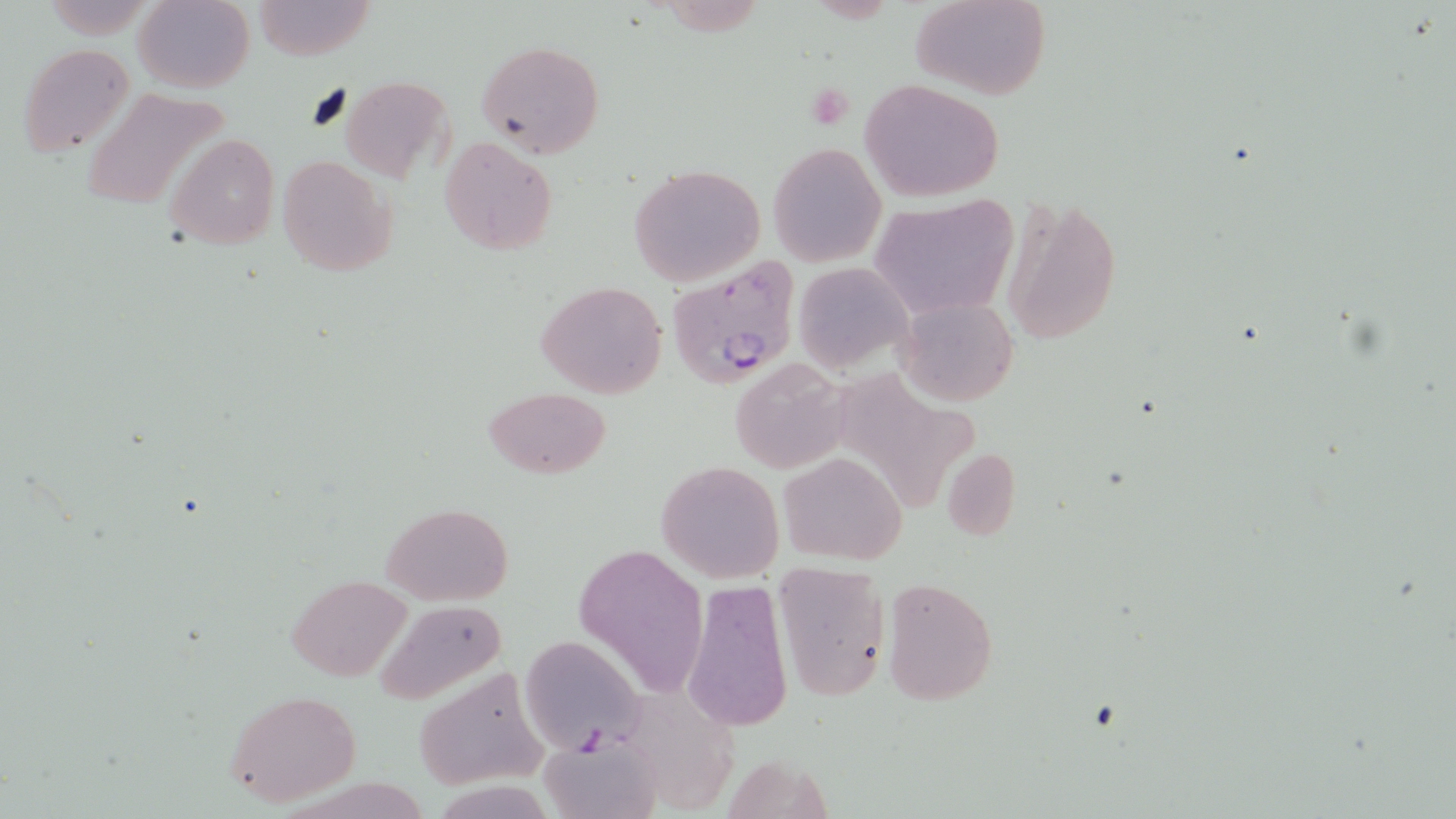
Summary:
  - Coordinate format: approximate bounding boxes as [x1, y1, x2, y2] in pixels
  - Plasmodium falciparum-infected red blood cell locations: [667, 259, 804, 389]
  - Uninfected red blood cell locations: [134, 0, 253, 91], [909, 0, 1053, 100], [251, 1, 374, 58], [475, 38, 605, 159], [17, 42, 136, 156], [337, 75, 453, 181], [861, 80, 1005, 203], [80, 88, 231, 211], [167, 133, 280, 250], [440, 138, 557, 254], [768, 143, 885, 266], [277, 154, 396, 278], [629, 164, 766, 287], [1001, 196, 1125, 346], [867, 197, 1019, 320], [795, 262, 910, 372], [536, 280, 666, 398], [895, 296, 1018, 406], [730, 361, 847, 475], [484, 387, 612, 477], [942, 446, 1021, 541], [779, 450, 906, 565], [655, 460, 785, 584], [381, 502, 514, 603], [574, 542, 709, 698], [770, 562, 891, 703], [882, 575, 998, 707], [287, 576, 411, 682], [681, 579, 793, 733], [372, 599, 510, 707], [520, 634, 646, 752], [413, 666, 550, 791], [223, 689, 363, 809], [541, 737, 660, 819]
  - Slide-level diagnosis: Plasmodium falciparum
  - Preparation: thin blood film
  - Field of view: one of a larger specimen
  - Image size: 1456×819 pixels
  - Modality: light microscopy
  - Magnification: 1000x
  - Stain: May-Grünwald-Giemsa